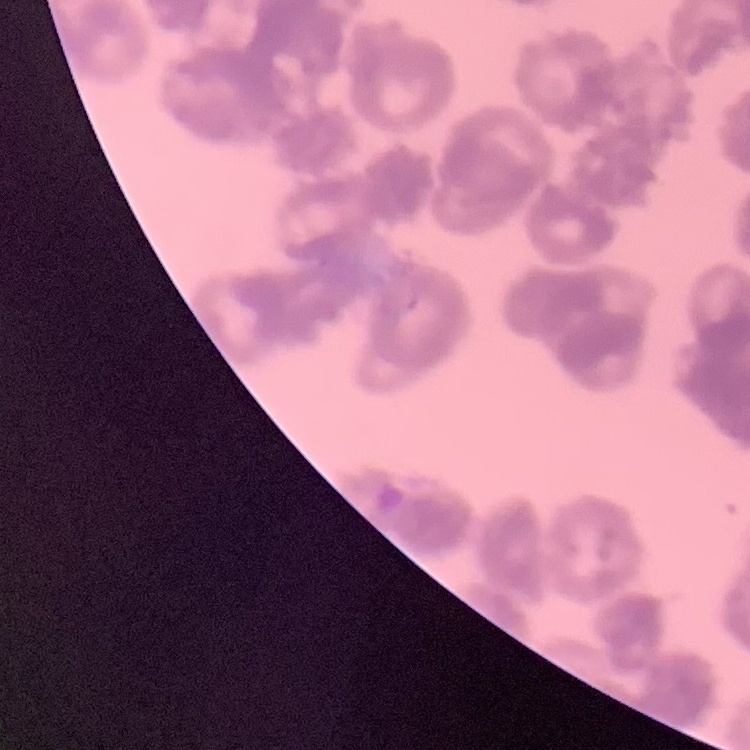
The red blood cells exhibit rouleaux formation. Field's or Giemsa stain. Thin blood smear. One tile cut from a larger photomicrograph.